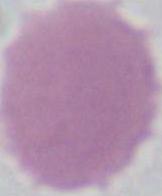 An erythrocyte is seen. Micrograph. 1000x magnification.